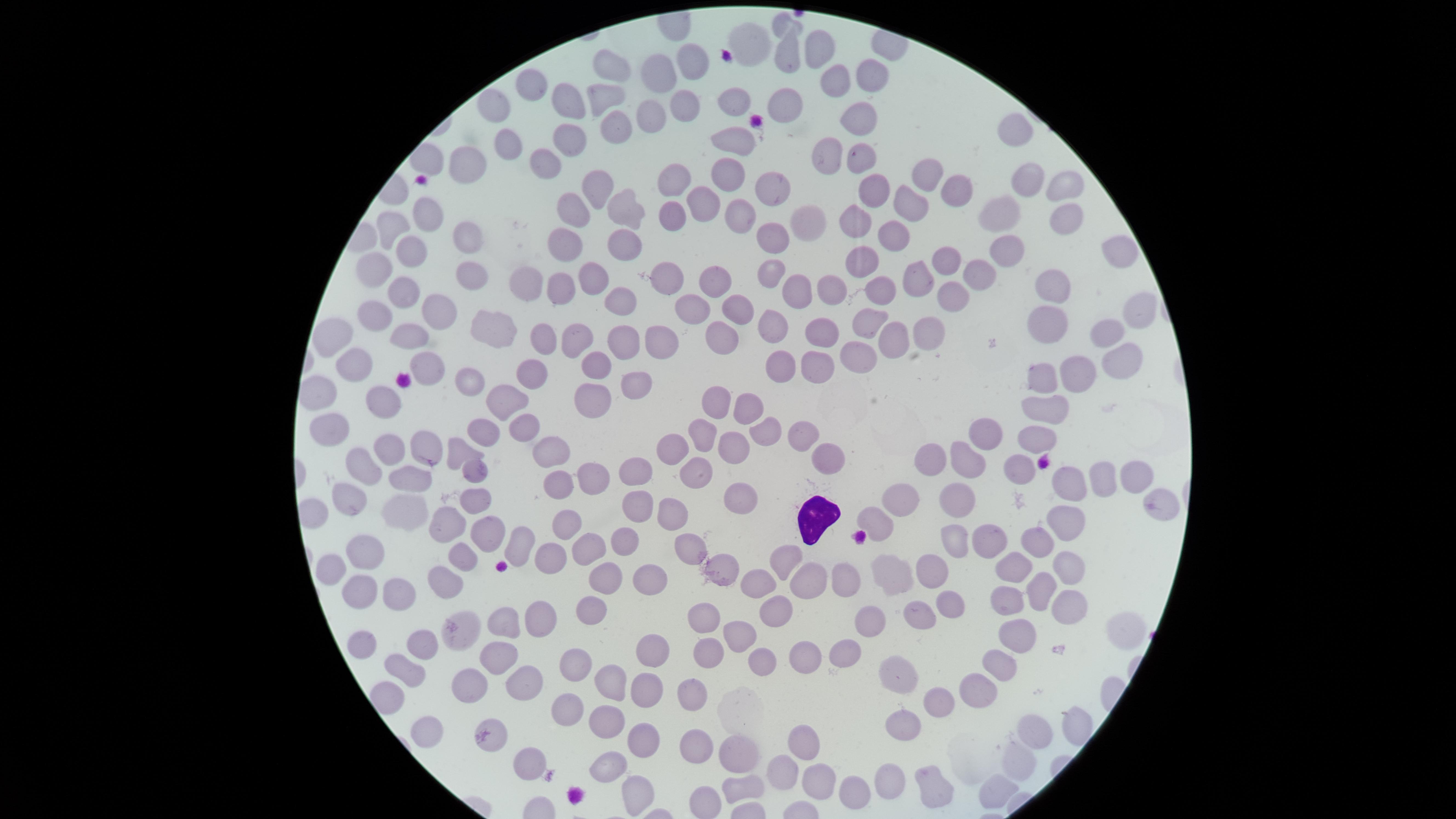 Approximate marker points as (x, y) in pixels. Uninfected red blood cells: (753, 38), (817, 52), (784, 53), (685, 59), (615, 69), (867, 74), (657, 78), (834, 78), (535, 86), (604, 94), (573, 100), (491, 103), (682, 106), (733, 107), (782, 108), (650, 122), (857, 123), (620, 130), (1020, 131), (509, 137), (572, 141), (735, 142), (826, 157), (859, 159), (543, 162), (466, 166), (923, 169), (733, 176), (669, 182), (1024, 182), (1067, 187), (961, 188), (595, 192), (775, 193), (871, 196), (707, 198), (910, 205), (427, 211), (624, 211), (1006, 213), (572, 214), (746, 218), (1058, 219), (672, 220), (850, 220), (806, 224), (392, 225), (892, 233), (776, 236), (624, 240), (466, 241), (569, 244), (408, 248), (1002, 249), (1112, 250), (947, 259), (864, 261), (373, 265), (977, 270), (922, 275), (663, 278), (768, 280), (527, 282), (595, 282), (473, 284), (881, 284), (1052, 285), (560, 287), (714, 287), (829, 288), (407, 293), (799, 294), (950, 296), (619, 298), (694, 304), (736, 306), (1139, 308), (439, 314), (374, 317), (868, 321), (1042, 323), (499, 326), (778, 327), (932, 334), (897, 335), (1109, 335), (330, 336), (722, 336), (824, 336), (542, 337), (575, 338), (409, 340), (655, 342), (622, 347), (860, 351), (355, 360), (816, 360), (1123, 360), (773, 364), (425, 366), (597, 367), (534, 371), (1076, 371), (468, 375), (643, 376), (1043, 380), (496, 396), (596, 401), (722, 401), (383, 402), (747, 403), (1041, 403), (330, 423), (522, 429), (772, 430), (708, 431), (801, 431), (488, 432), (985, 435), (1030, 441), (421, 447), (460, 448), (550, 449), (673, 451), (390, 452), (729, 454), (938, 456), (824, 457), (970, 459), (1021, 465), (370, 466), (473, 469), (698, 469), (641, 470), (1099, 471), (596, 474), (1135, 474), (408, 475), (1072, 476), (559, 486), (475, 491), (734, 492), (951, 492), (899, 497), (636, 498), (1160, 499), (344, 502), (401, 505), (674, 513), (876, 518), (567, 520), (450, 524), (1064, 525), (487, 530), (955, 536), (623, 537), (990, 537), (1033, 537), (518, 542), (587, 546), (688, 546), (361, 550), (463, 555), (552, 557), (792, 559), (1015, 559), (329, 563), (1069, 566), (888, 571), (932, 571), (716, 572), (649, 573), (606, 575), (808, 580), (845, 580), (445, 581), (755, 582), (395, 591), (356, 592), (1041, 592), (1007, 599), (953, 605), (587, 607), (772, 607), (1067, 607), (918, 614), (546, 617), (868, 618), (506, 620), (700, 620), (1127, 627), (463, 628), (739, 633), (1015, 634), (361, 638), (424, 646), (844, 647), (708, 650), (655, 654), (490, 656), (797, 659), (759, 660), (1000, 661), (575, 664), (407, 665), (892, 671), (469, 679), (520, 681), (611, 683), (643, 685), (689, 688), (976, 689), (564, 698), (939, 699), (899, 723), (1075, 724), (605, 726), (429, 729), (1037, 734), (795, 736), (491, 737), (640, 737), (691, 742), (730, 750), (1021, 757), (527, 759), (614, 765), (783, 769), (814, 773), (890, 780), (994, 785), (739, 786), (927, 786), (852, 789), (640, 790). White blood cells: (813, 517). Giemsa stain. Image is 1456×819 pixels. The visible region is circular. Presence: no malaria parasites detected. One field of view of the specimen. Thin blood film. Photographed with a smartphone camera through the microscope eyepiece.